Comment on the morphology of the red blood cells.
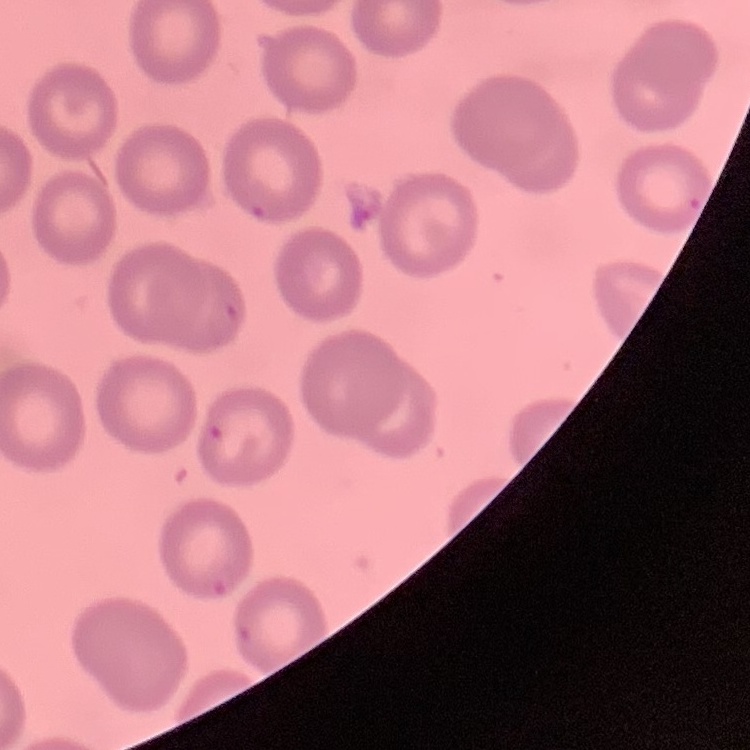

No rouleaux formation.

One tile cut from a larger photomicrograph. Stained with either Field's or Giemsa. Thin peripheral smear.